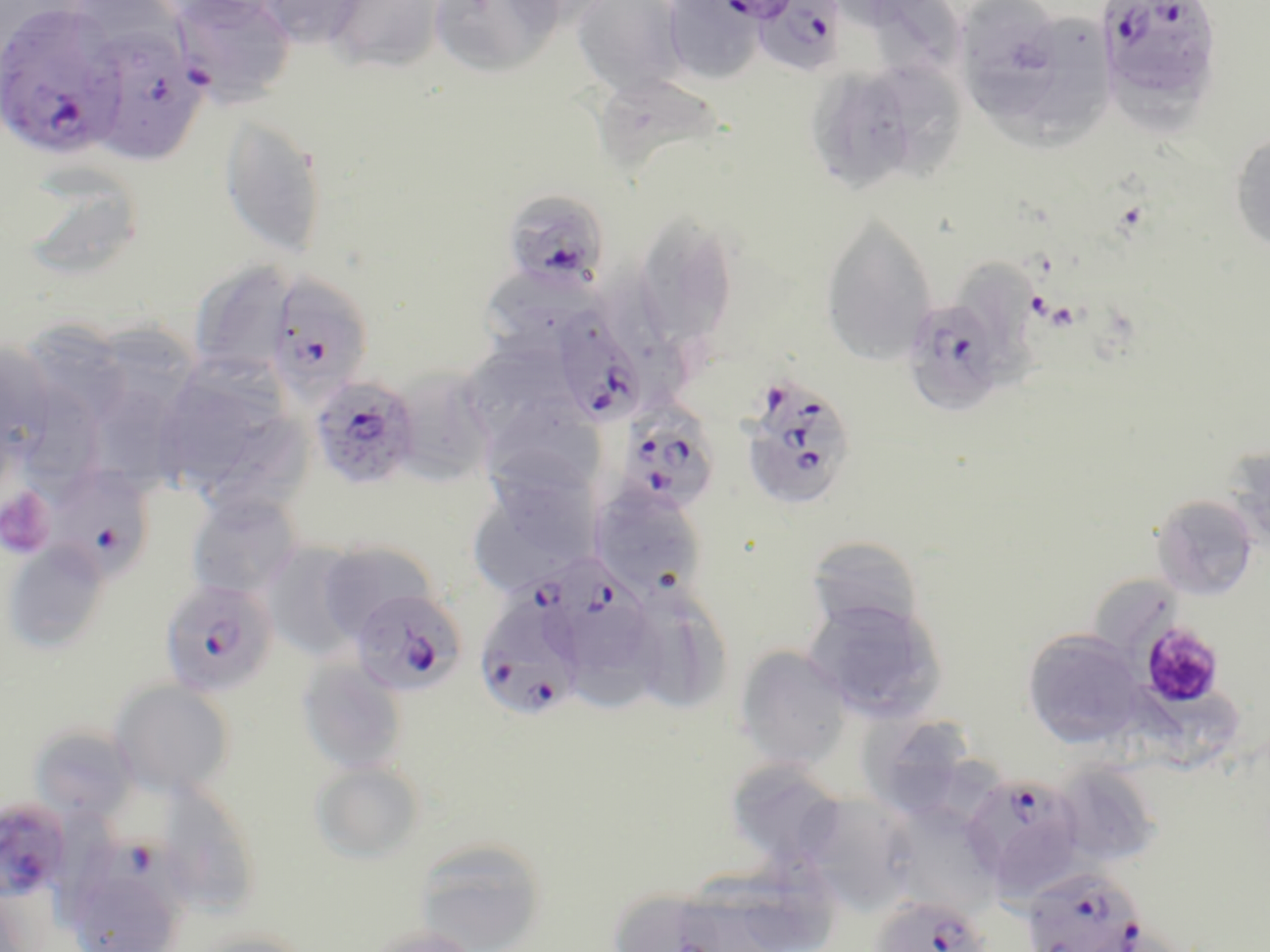

Approximate bounding boxes as (x1,y1)-(x2,y2) corner pairs in pixels. Uninfected red blood cell locations (subset): (252,0)-(368,49), (325,0)-(445,73), (428,0)-(563,78), (571,0)-(688,97), (662,0)-(762,84), (956,0)-(1067,105), (1020,7)-(1117,138), (802,62)-(950,194), (591,73)-(729,183), (219,115)-(328,258), (1229,130)-(1270,255), (11,163)-(148,284), (632,214)-(739,349), (819,216)-(937,366), (963,257)-(1046,388), (188,258)-(296,381), (479,274)-(599,357), (97,315)-(201,472), (24,321)-(129,431), (1,336)-(56,463), (152,358)-(306,507), (393,368)-(504,489), (23,381)-(114,500), (490,392)-(610,489), (1225,442)-(1270,553), (488,451)-(604,561), (589,485)-(709,602), (186,492)-(302,599), (473,494)-(596,589), (1151,495)-(1258,600), (804,536)-(926,640), (1,540)-(111,655), (315,540)-(440,641), (260,541)-(368,655), (1095,580)-(1190,651), (637,582)-(728,711), (805,597)-(946,721), (571,607)-(667,715), (1022,628)-(1147,748), (733,645)-(853,770), (296,657)-(409,776), (108,680)-(236,798), (1109,684)-(1252,766), (859,704)-(968,804), (29,723)-(137,821), (724,757)-(850,869), (310,761)-(425,863), (1051,761)-(1164,868), (153,784)-(264,919), (793,792)-(920,913), (883,807)-(1007,921), (414,837)-(548,952), (746,845)-(844,950), (678,875)-(777,952), (0,882)-(43,952), (616,887)-(728,951), (361,924)-(481,952), (188,930)-(312,952). Platelet locations: (0,486)-(56,559), (1138,621)-(1226,709). Plasmodium falciparum-infected red blood cell locations (subset): (169,0)-(297,107), (714,0)-(802,24), (750,0)-(847,77), (1095,0)-(1224,110), (0,2)-(124,159), (85,25)-(208,166), (501,189)-(610,292), (266,274)-(374,401), (901,296)-(1010,415), (551,306)-(650,427), (309,373)-(421,490), (741,375)-(859,513), (615,403)-(721,517), (44,463)-(155,582), (512,549)-(652,669), (158,578)-(280,699), (350,588)-(467,697), (474,590)-(587,722), (961,772)-(1085,896), (0,798)-(72,900), (1020,867)-(1146,951), (869,894)-(992,952). Slide-level diagnosis: Plasmodium falciparum. Thin blood smear. One field of a larger specimen. Light microscopy. May-Grünwald-Giemsa-stained preparation. Image is 1270×952 pixels. 1000x magnification.